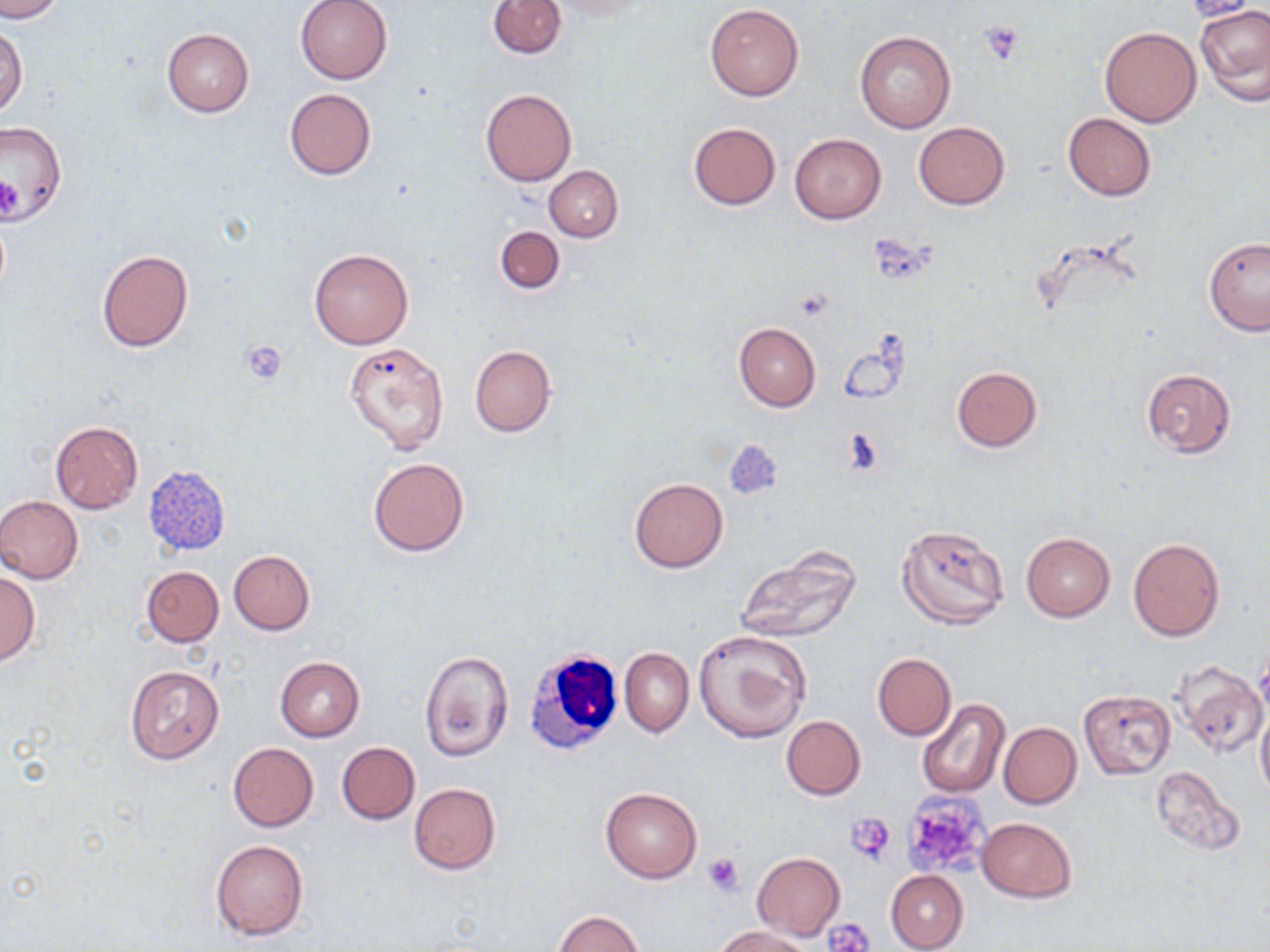
slide-level diagnosis = negative for blood parasites
preparation = thin blood film
white blood cell locations = approximate bounding boxes as (x1,y1)-(x2,y2) corner pairs in pixels: (522,645)-(627,758)
field of view = one of a larger specimen
magnification = 1000x
uninfected red blood cell locations = approximate bounding boxes as (x1,y1)-(x2,y2) corner pairs in pixels: (1,0)-(68,22), (296,0)-(393,84), (486,0)-(567,58), (537,0)-(653,18), (1179,1)-(1260,21), (706,4)-(805,100), (1195,4)-(1270,106), (1,25)-(28,118), (1099,26)-(1200,126), (162,28)-(254,117), (855,30)-(955,133), (285,88)-(375,180), (480,89)-(577,186), (1062,113)-(1156,200), (0,119)-(70,223), (912,120)-(1011,210), (688,123)-(780,208), (789,133)-(886,224), (544,165)-(623,241), (494,225)-(565,294), (1203,237)-(1270,337), (308,247)-(414,349), (96,250)-(194,352), (734,322)-(821,410), (345,343)-(450,455), (469,344)-(556,437), (951,366)-(1042,451), (1141,368)-(1237,458), (50,421)-(143,514), (369,458)-(469,555), (142,465)-(230,557), (629,477)-(727,571), (0,495)-(84,584), (895,523)-(1008,629), (1021,532)-(1114,622), (1127,538)-(1224,641), (734,546)-(862,643), (228,551)-(315,635), (140,566)-(223,646), (0,567)-(38,665), (693,630)-(811,743), (621,648)-(694,737), (420,650)-(513,761), (873,653)-(956,740), (275,656)-(364,742), (1170,662)-(1267,758), (125,665)-(223,764), (1078,689)-(1175,778), (915,699)-(1009,799), (1256,703)-(1270,802), (781,715)-(865,800), (998,721)-(1082,810), (337,742)-(419,824), (227,743)-(319,832), (1149,767)-(1243,852), (408,783)-(501,875), (600,787)-(702,883), (976,817)-(1078,903), (211,840)-(308,941), (752,852)-(845,941), (885,869)-(968,952), (553,910)-(645,951), (715,925)-(814,952)
stain = May-Grünwald-Giemsa
image size = 1270×952 pixels
modality = optical microscopy
platelet locations = approximate bounding boxes as (x1,y1)-(x2,y2) corner pairs in pixels: (979,21)-(1025,65), (0,174)-(22,224), (867,234)-(938,286), (795,287)-(834,321), (239,340)-(289,385), (841,430)-(885,474), (898,792)-(992,879), (845,811)-(896,865), (703,853)-(744,894), (826,918)-(873,951)